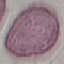 Result: no malaria parasites detected. Acquired by smartphone through the microscope eyepiece. Automatically extracted cell patch, resized to 64 × 64 pixels. Thin blood film. Giemsa stain.